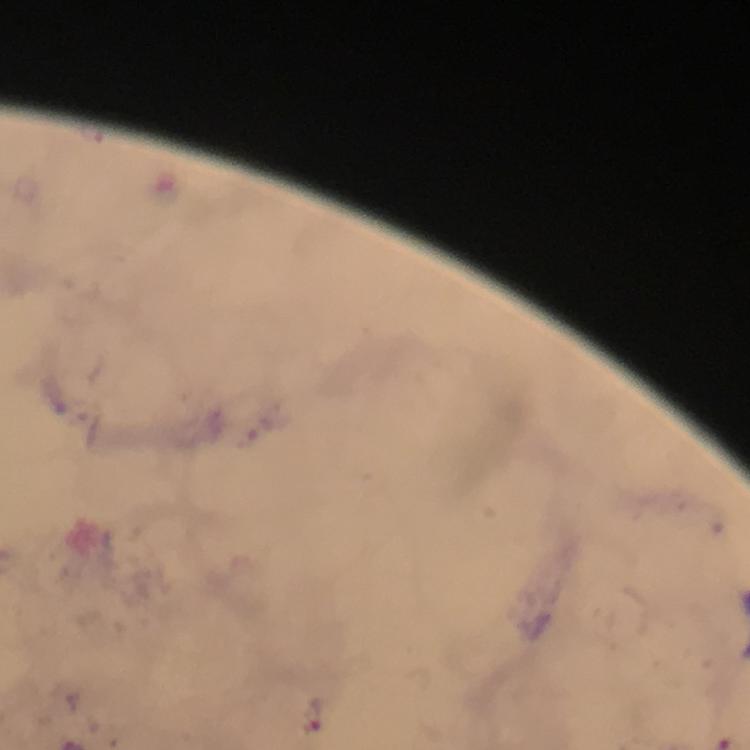

Approximate centers as {x, y} in pixels. Plasmodium parasite locations: {264, 429}, {314, 713}. Immersion oil was used. Thick smear. From a malaria diagnostic workup. Giemsa stain. Photographed through the microscope with a smartphone camera. Cropped region of a single field of view. At 100x magnification. Image is 750×750 pixels.